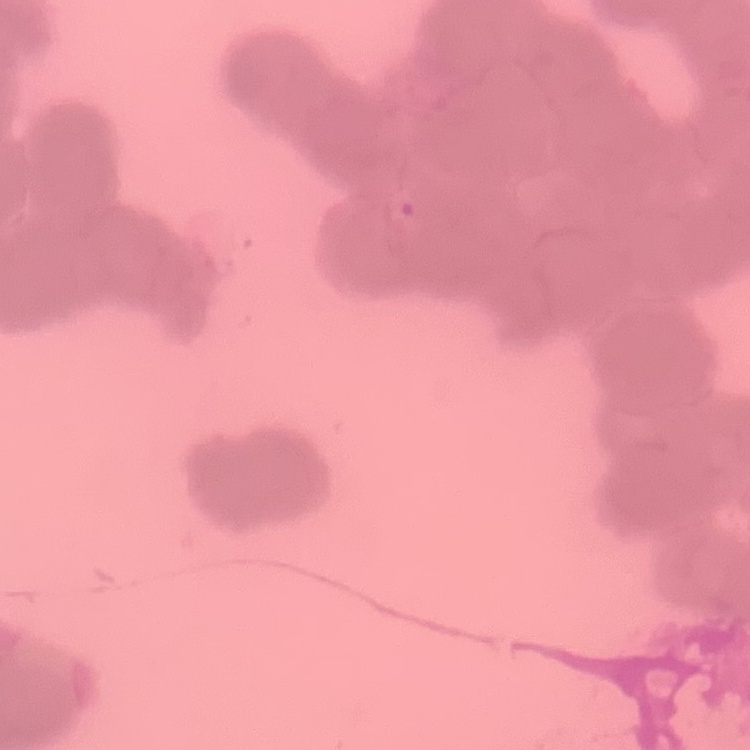
The red blood cells exhibit rouleaux formation. Thin blood smear. Stained with either Field's or Giemsa. Square crop of a larger photomicrograph.